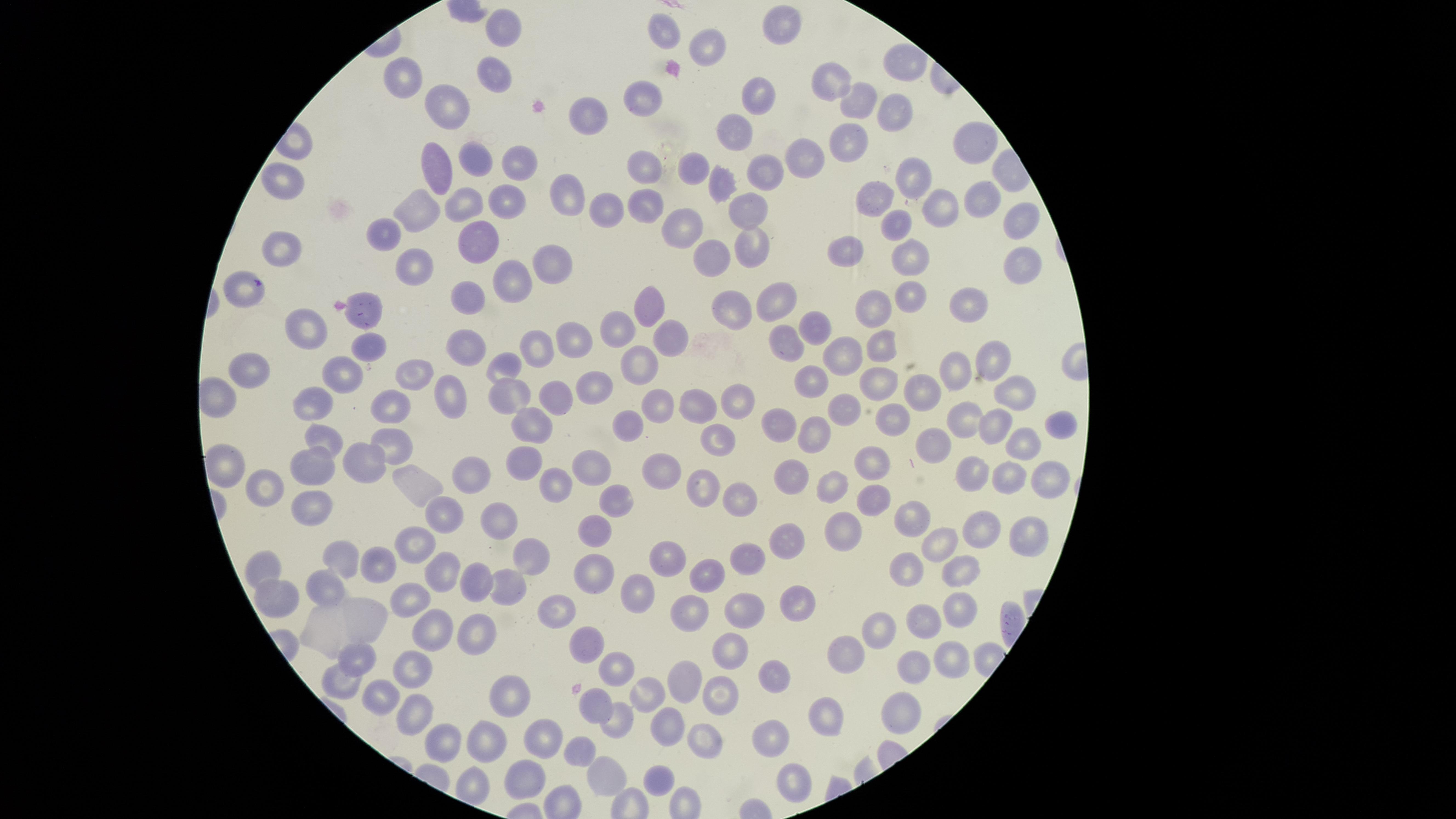
Approximate marker points as (x, y) in pixels. Uninfected RBCs: (780, 26), (504, 28), (662, 32), (705, 46), (492, 73), (832, 74), (410, 80), (756, 94), (641, 100), (449, 103), (852, 106), (894, 112), (587, 114), (735, 138), (849, 142), (971, 145), (433, 156), (805, 160), (517, 162), (479, 165), (651, 167), (695, 167), (761, 173), (910, 179), (279, 182), (722, 187), (880, 193), (565, 197), (975, 198), (507, 200), (464, 202), (424, 204), (644, 206), (751, 207), (937, 207), (597, 210), (1024, 220), (686, 226), (891, 227), (386, 233), (477, 244), (753, 246), (848, 252), (284, 255), (897, 255), (716, 256), (414, 261), (546, 264), (1022, 266), (509, 287), (241, 295), (918, 295), (472, 297), (965, 300), (779, 302), (652, 303), (882, 307), (736, 312), (365, 317), (305, 327), (816, 327), (618, 331), (667, 333), (577, 338), (372, 344), (786, 344), (879, 344), (467, 348), (529, 352), (839, 358), (987, 362), (505, 368), (640, 372), (251, 374), (954, 376), (417, 377), (339, 378), (814, 381), (884, 381), (596, 388), (1014, 391), (923, 392), (508, 393), (447, 394), (559, 394), (739, 397), (314, 401), (694, 401), (658, 405), (849, 405), (393, 410), (896, 417), (968, 418), (532, 422), (632, 424), (1059, 424), (990, 425), (778, 427), (817, 429), (720, 436), (329, 438), (391, 443), (1015, 443), (936, 449), (228, 462), (876, 462), (519, 464), (367, 465), (317, 469), (471, 469), (593, 469), (668, 471), (975, 474), (1011, 474), (1048, 477), (795, 478), (267, 482), (556, 483), (835, 484), (417, 485), (699, 488), (612, 497), (875, 500), (744, 503), (310, 504), (443, 509), (913, 521), (497, 523), (848, 528), (595, 529), (982, 531), (1030, 539), (788, 541), (937, 542), (415, 546), (342, 556), (532, 556), (667, 557), (741, 559), (379, 564), (959, 565), (444, 567), (260, 569), (910, 569), (592, 572), (706, 576), (478, 581), (504, 584), (330, 589), (636, 589), (286, 597), (410, 597), (792, 600), (743, 604), (959, 605), (684, 608), (561, 609), (372, 615), (882, 620), (923, 623), (437, 625), (472, 630), (322, 632), (588, 642), (853, 650), (733, 651), (359, 654), (950, 654), (614, 665), (913, 665), (775, 669), (413, 670), (689, 679), (338, 686), (653, 691), (722, 698), (377, 699), (600, 700), (508, 702), (902, 709), (413, 712), (825, 715), (615, 720), (671, 727), (707, 731), (540, 738), (778, 738), (445, 743), (584, 745), (486, 747), (607, 776), (791, 776), (518, 778), (660, 779). Circular visible region. Photographed with a smartphone camera through the microscope eyepiece. Presence: no malaria parasites identified. Image is 1456×819 pixels. Thin smear of blood. Single field of view. Giemsa stain.